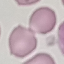

Summary:
  - Result: no malaria parasites seen
  - Stain: Giemsa
  - Capture: smartphone camera at the microscope eyepiece
  - Image type: automatically extracted cell patch, resized to 64 × 64 pixels
  - Preparation: thin smear